Assess the morphology of the red blood cells.
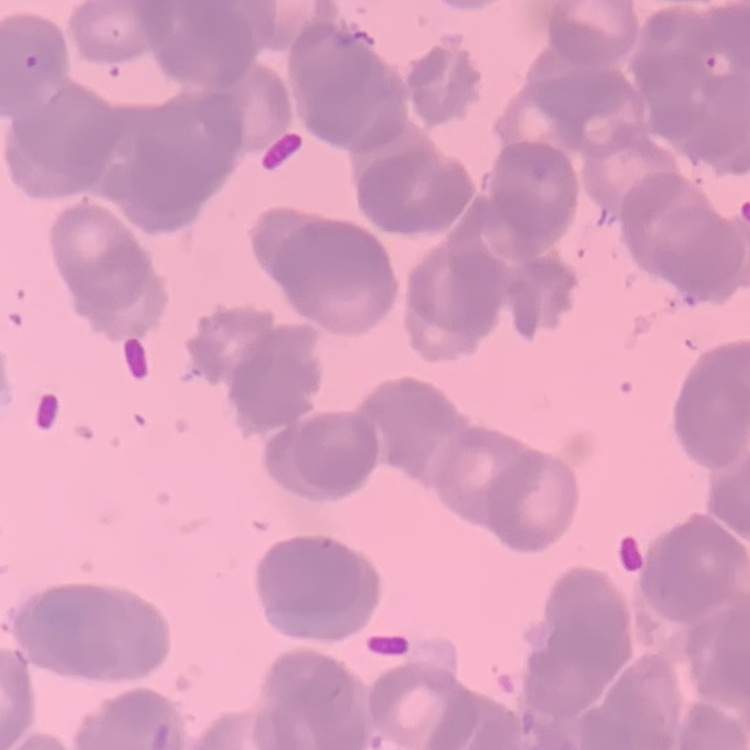

They show rouleaux formation.

Thin peripheral smear. Square crop of a larger photomicrograph. Stained with either Field's or Giemsa.